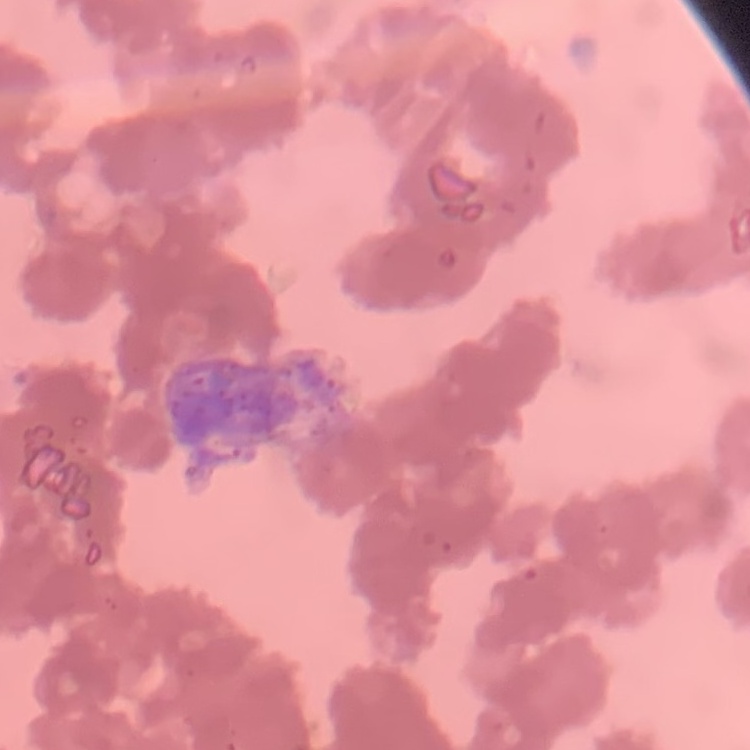

The erythrocytes exhibit rouleaux formation. One tile cut from a larger photomicrograph. Field's or Giemsa stain. Thin peripheral smear.